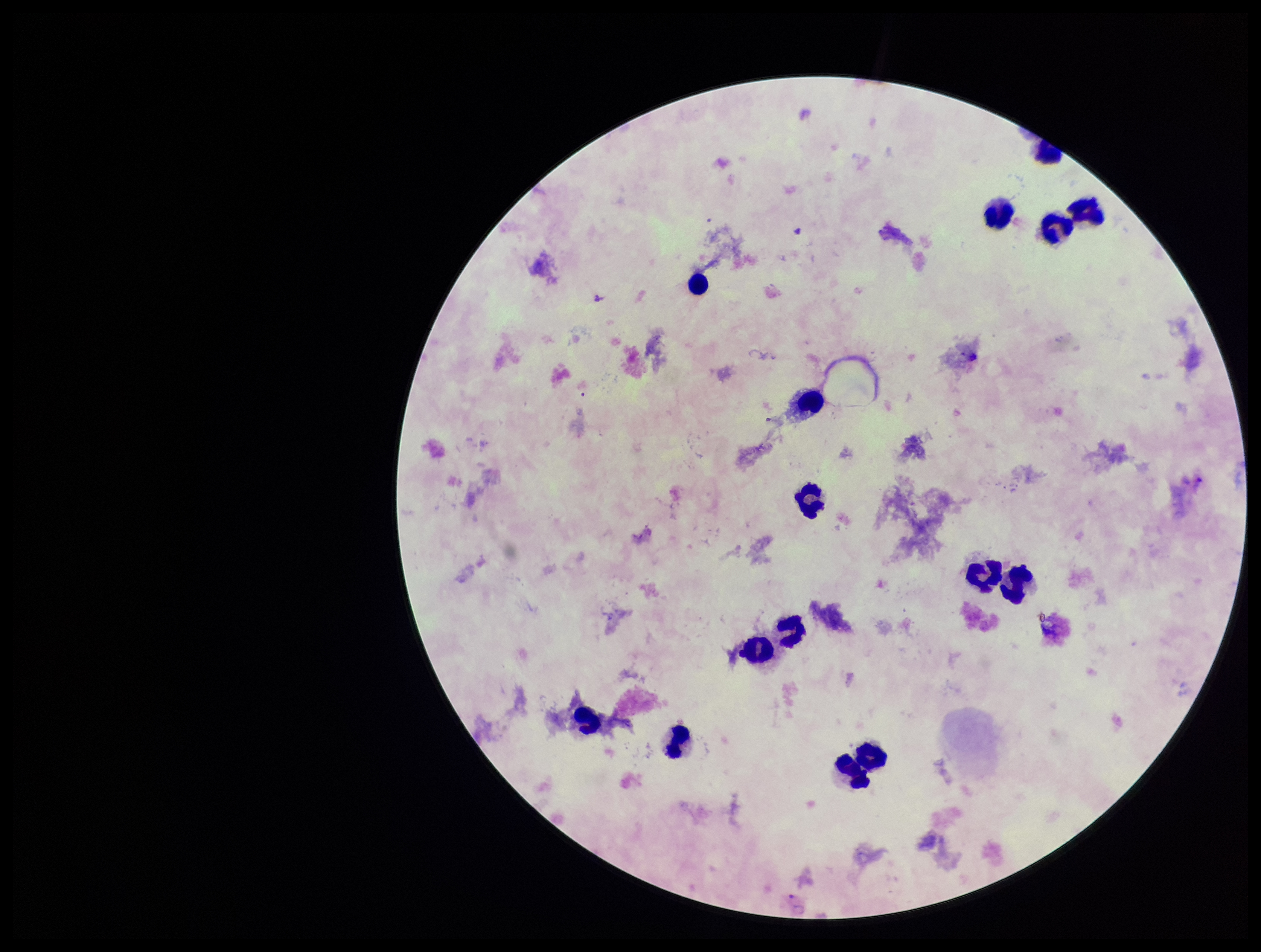
Summary:
  - Leukocyte count: 15
  - Stain: Giemsa
  - Patient malaria status: infected
  - Plasmodium parasites: none seen
  - Field of view: one from this slide
  - Image size: 1261×952 pixels
  - Capture: smartphone photograph through the microscope eyepiece
  - Preparation: thick blood smear
  - Parasite count: 0
  - Species reported for this patient: Plasmodium vivax